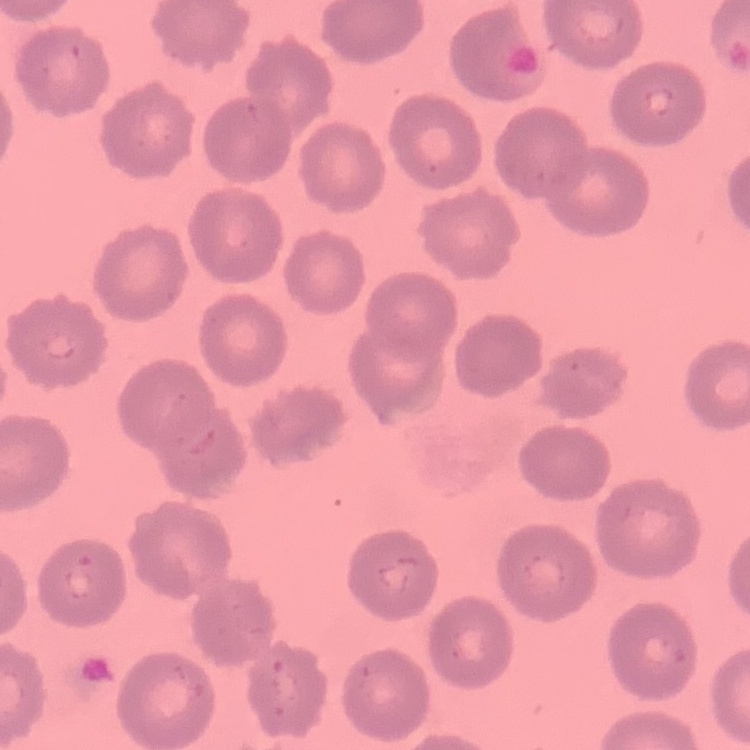
The red blood cells exhibit no rouleaux formation. Stained with either Field's or Giemsa. Thin peripheral smear. One tile cut from a larger photomicrograph.